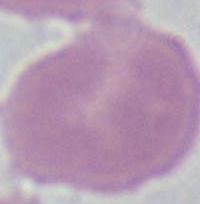

Summary:
  - Identification: red blood cell
  - Magnification: 1000x
  - Modality: micrograph